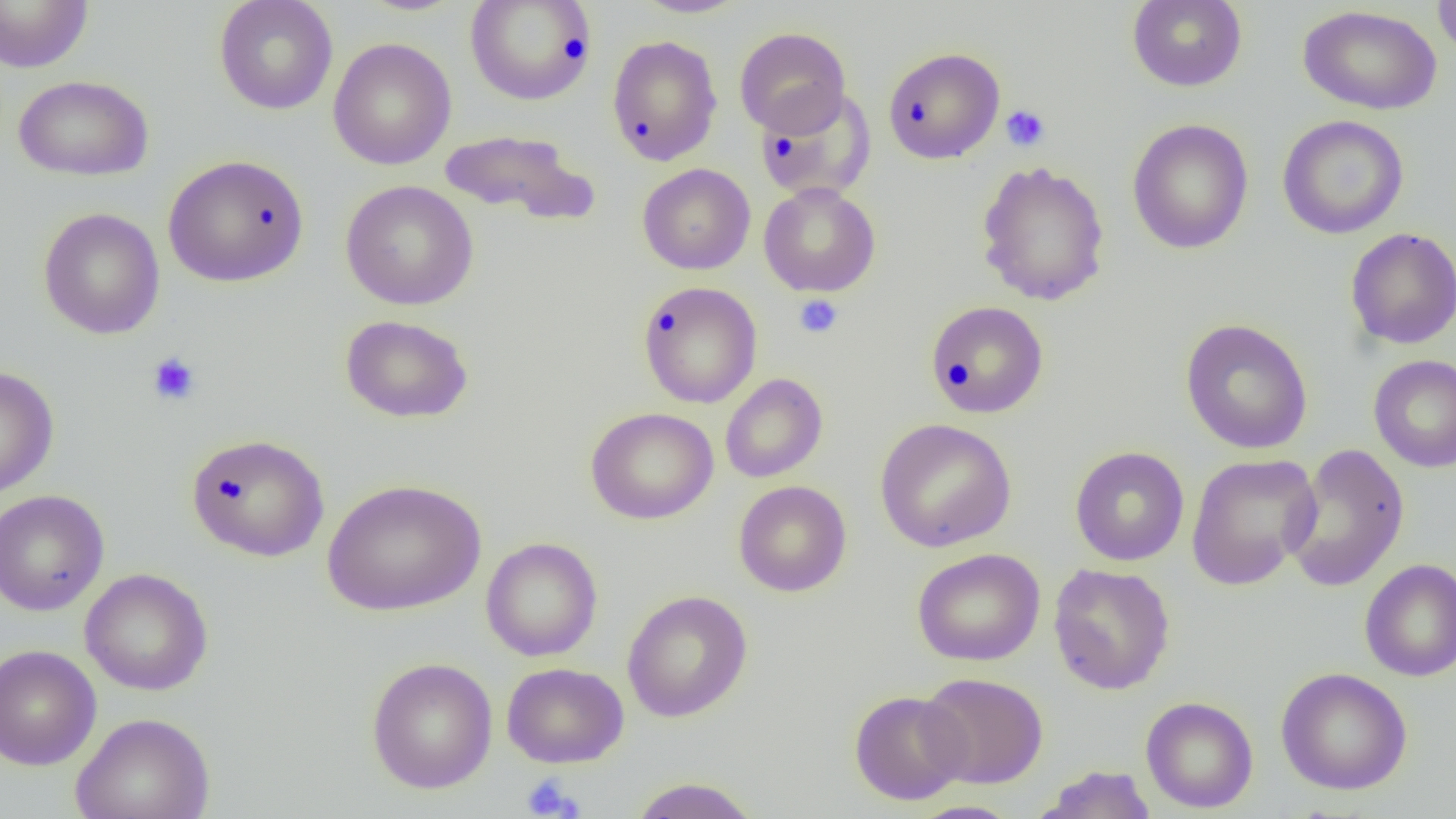 Approximate bounding boxes as [x1, y1, x2, y2] in pixels. Platelet locations: [1001, 104, 1051, 152], [794, 294, 844, 339], [146, 352, 201, 406], [521, 773, 583, 818]. Uninfected red blood cell locations: [213, 0, 338, 115], [465, 0, 598, 105], [634, 0, 749, 18], [1127, 0, 1248, 91], [1433, 0, 1456, 58], [0, 1, 93, 73], [1299, 5, 1442, 115], [734, 26, 851, 137], [607, 34, 723, 166], [328, 37, 456, 170], [883, 46, 1005, 164], [13, 74, 154, 181], [755, 86, 876, 202], [1277, 115, 1409, 239], [1127, 118, 1254, 254], [438, 128, 599, 226], [162, 154, 309, 288], [975, 160, 1110, 306], [637, 163, 756, 275], [340, 180, 479, 311], [758, 182, 881, 297], [38, 207, 165, 339], [1345, 227, 1456, 350], [638, 281, 762, 408], [925, 300, 1049, 419], [340, 314, 474, 424], [1180, 318, 1313, 454], [1369, 354, 1456, 473], [0, 365, 59, 498], [719, 373, 828, 483], [586, 407, 719, 524], [874, 418, 1016, 552], [186, 433, 330, 562], [1282, 443, 1411, 593], [1070, 446, 1189, 566], [1185, 453, 1323, 590], [322, 478, 487, 616], [733, 480, 851, 597], [0, 489, 110, 616], [481, 537, 602, 661], [912, 548, 1045, 666], [1360, 559, 1456, 681], [1048, 563, 1175, 695], [80, 568, 213, 695], [622, 590, 753, 722], [0, 644, 101, 771], [366, 657, 498, 794], [502, 662, 629, 768], [1276, 667, 1413, 795], [918, 672, 1049, 789], [848, 690, 971, 805], [1141, 696, 1258, 813], [70, 711, 215, 819], [1033, 765, 1157, 818], [628, 776, 760, 819], [905, 800, 1025, 819]. Slide-level diagnosis: negative for blood parasites. Captured at 1000x magnification. Light microscopy. One field of a larger specimen. Image is 1456×819 pixels. Thin blood smear.